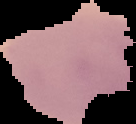

{
  "preparation": "thin blood smear",
  "result": "Plasmodium parasites identified",
  "image_type": "segmented cell region on a black background",
  "image_size": "136×124 pixels"
}